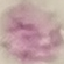

Summary:
  - Result: no malaria parasites detected
  - Preparation: thin smear
  - Image type: cell patch, automatically extracted from a larger field of view and resized to 64 × 64 pixels
  - Capture: smartphone camera at the microscope eyepiece
  - Stain: Giemsa